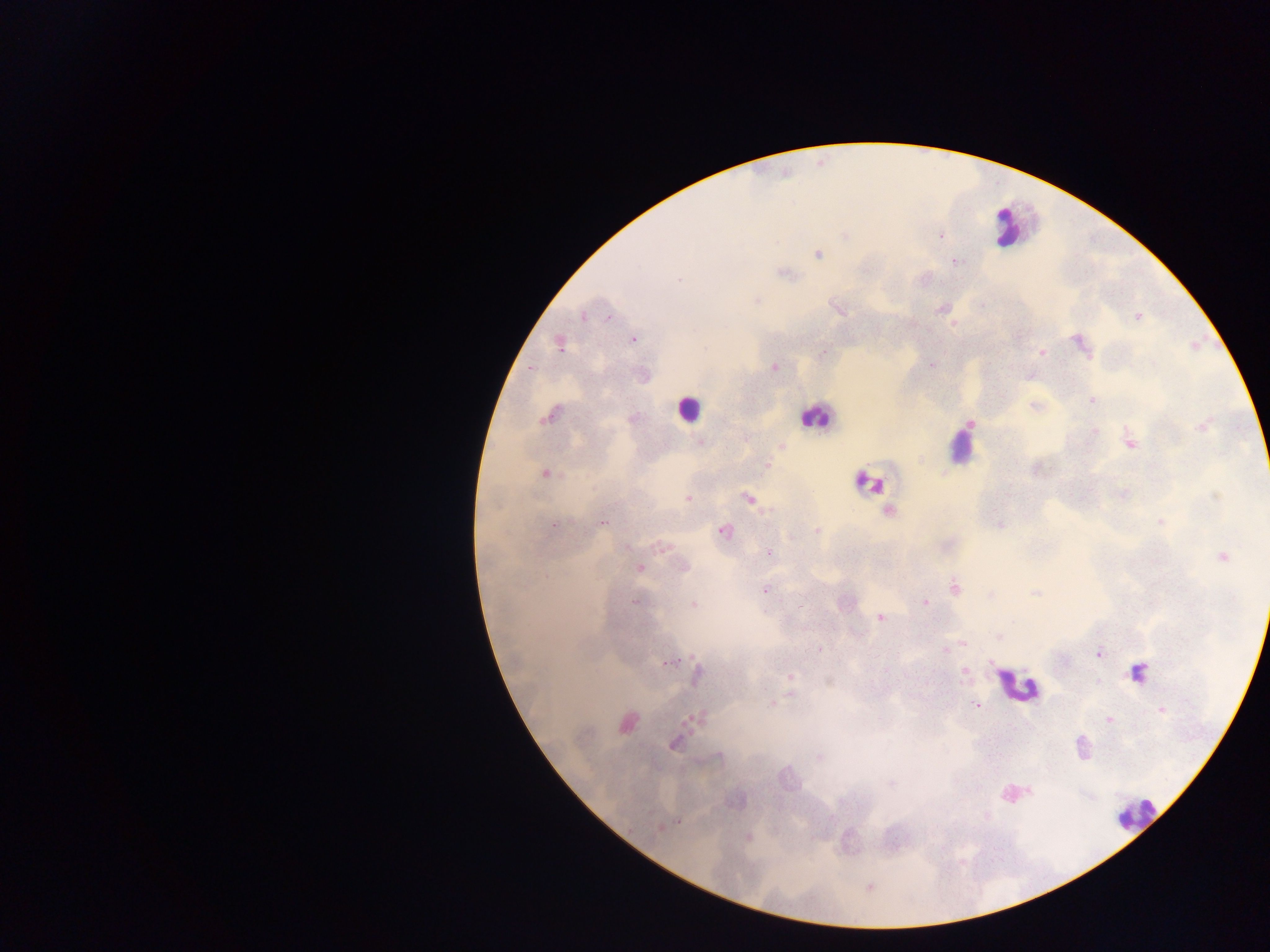
leukocyte locations = approximate centers as [x, y] in pixels: [1006, 225], [687, 409], [813, 415], [959, 447], [868, 482], [1138, 672], [1017, 685], [1136, 815]
Plasmodium parasite locations = approximate centers as [x, y] in pixels: [845, 236], [940, 236], [817, 254], [955, 262], [785, 273], [679, 279], [756, 301], [941, 309], [841, 311], [583, 317], [610, 317], [1137, 317], [633, 340], [1080, 343], [559, 345], [705, 348], [823, 352], [1042, 352], [931, 365], [774, 367], [1092, 400], [548, 416], [970, 423], [1202, 425], [1094, 431], [700, 442], [1130, 443], [781, 446], [765, 465], [545, 474], [1215, 497], [687, 498], [748, 499], [889, 511], [1160, 522], [602, 523], [554, 525], [1001, 525], [817, 530], [723, 531], [626, 546], [660, 547], [768, 554], [1222, 556], [684, 566], [639, 569], [955, 588], [765, 590], [1034, 593], [990, 595], [636, 602], [925, 603], [693, 604], [880, 618], [1000, 637], [963, 643], [819, 649], [945, 650], [1099, 653], [668, 662], [965, 672], [696, 674], [791, 677], [790, 695], [771, 704], [976, 705], [1162, 709], [697, 719], [1109, 719], [626, 722], [673, 744], [718, 756], [819, 758], [890, 784], [1030, 791], [678, 822], [659, 827], [748, 838]
preparation = thick blood smear
image size = 1270×952 pixels
country = Ghana
field of view = single
capture = mobile-phone photograph through a microscope